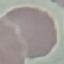
result: no malaria parasites seen
capture: smartphone through the microscope eyepiece
image_type: cell patch, automatically extracted from a larger field of view and resized to 64 × 64 pixels
stain: Giemsa
preparation: thin blood smear